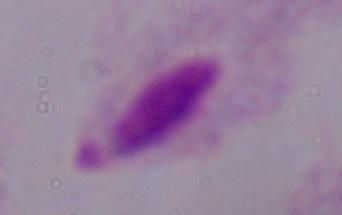

Summary:
  - Modality: micrograph
  - Magnification: 1000x
  - Identification: trichomonad